Describe the morphology of the erythrocytes.
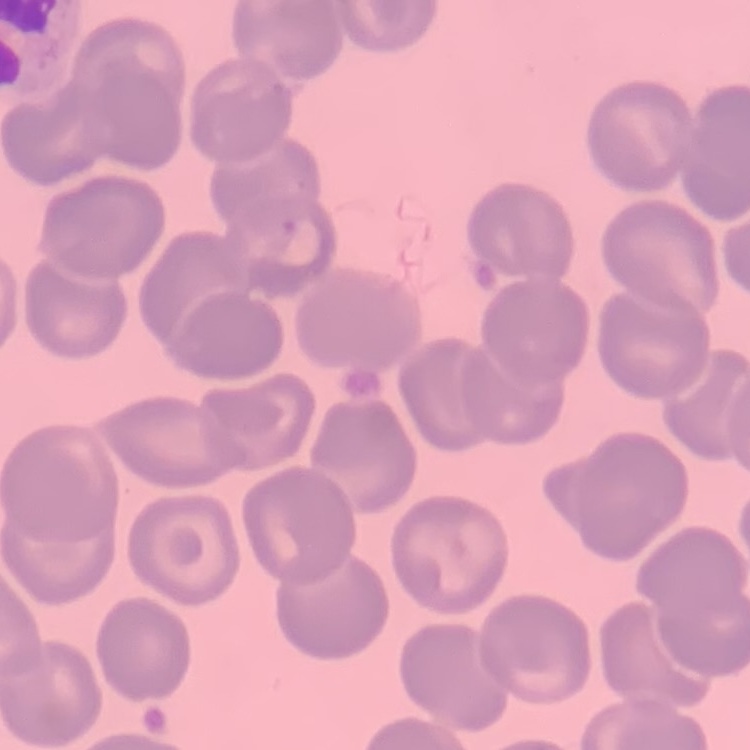

No rouleaux formation.

One tile cut from a larger photomicrograph. Thin blood smear. Field's or Giemsa stain.